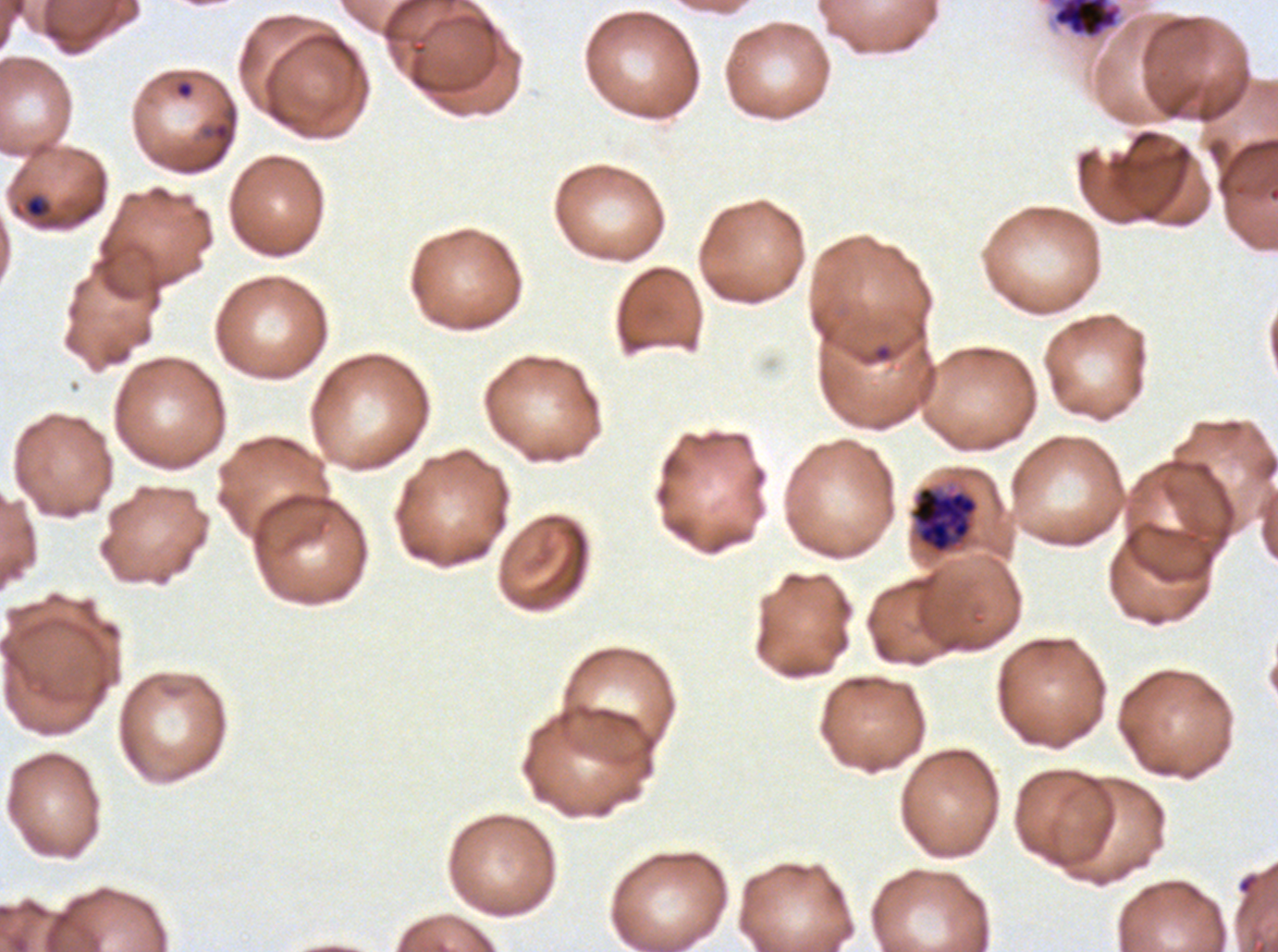
Approximate bounding rectangles given as corner coordinates in pixels from the top-left. Late schizont locations: (x1=1051, y1=0, x2=1123, y2=40). Early schizont locations: (x1=912, y1=486, x2=977, y2=553). Late-ring/early-trophozoite locations: (x1=13, y1=191, x2=54, y2=221). Ring locations: (x1=174, y1=79, x2=194, y2=100). P. falciparum cultured ex vivo for 24 to 48 hours, from a patient in The Gambia. Thin blood film. One sub-image of a larger composite. Giemsa stain. Life-cycle stages observed: ring, late-ring/early-trophozoite, early schizont, late schizont. Image is 1278×952 pixels.